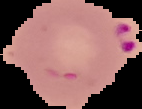
image_type: segmented cell region on a black background
image_size: 142×109 pixels
malaria_status: parasitized
preparation: thin blood film